Identify the cell.
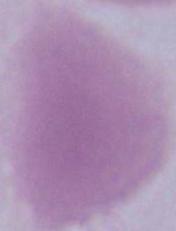
An erythrocyte.

magnification = 1000x
modality = photomicrograph